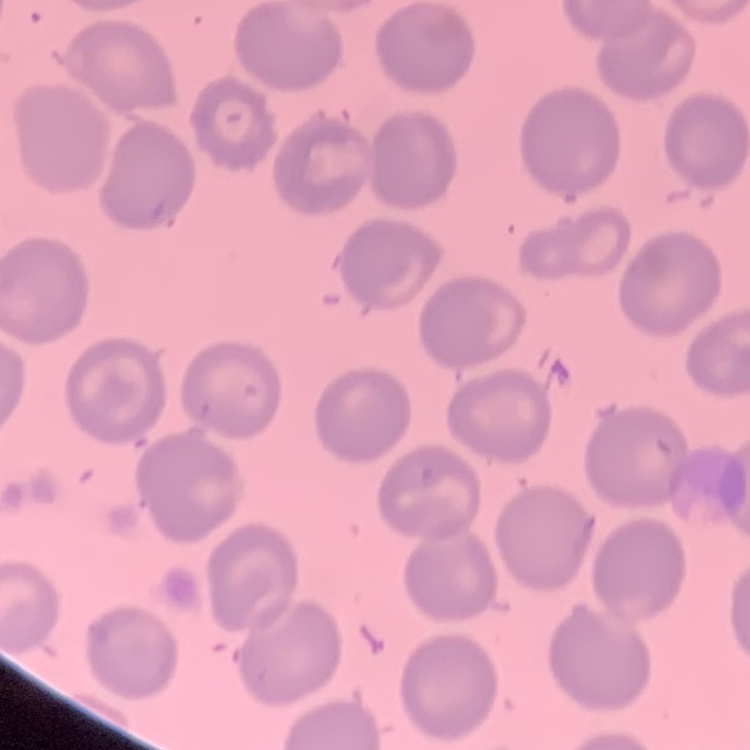

The erythrocytes exhibit no rouleaux formation. Thin blood film. Field's or Giemsa stain. Square crop of a larger photomicrograph.